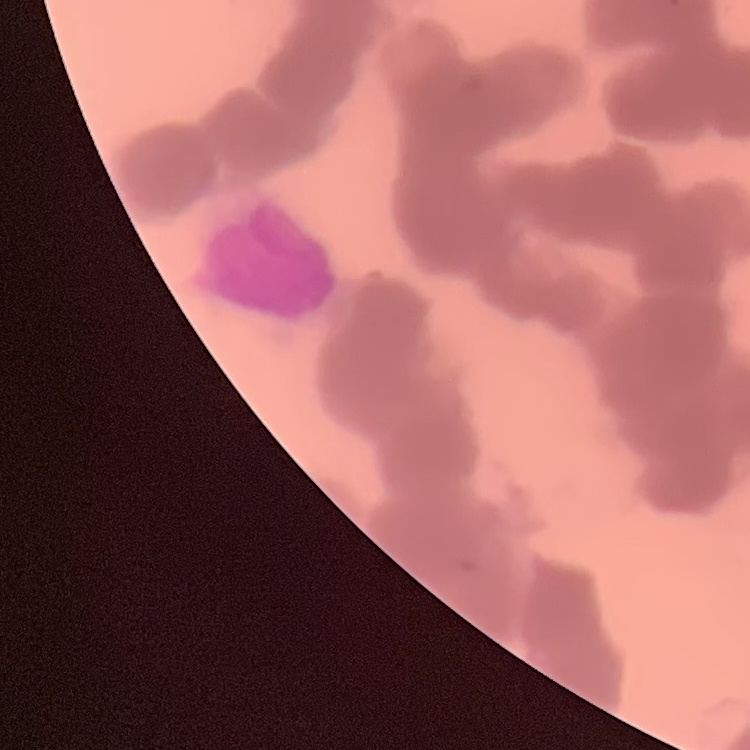

Summary:
  - Erythrocyte morphology: rouleaux formation
  - Stain: Field's or Giemsa
  - Preparation: thin peripheral smear
  - Image type: one tile cut from a larger photomicrograph